Assess this cell for malaria.
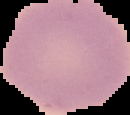

It is uninfected.

image size = 130×115 pixels
preparation = thin blood film
image type = segmented cell region with the area outside set to black